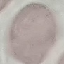

Summary:
  - Malaria status: uninfected
  - Stain: Giemsa
  - Capture: smartphone through the microscope eyepiece
  - Image type: cell patch, automatically extracted from a larger field of view and resized to 64 × 64 pixels
  - Preparation: thin smear